Identify the parasite.
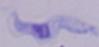

This is a trypanosome.

Summary:
  - Modality: photomicrograph
  - Magnification: 1000x